Identify the parasite.
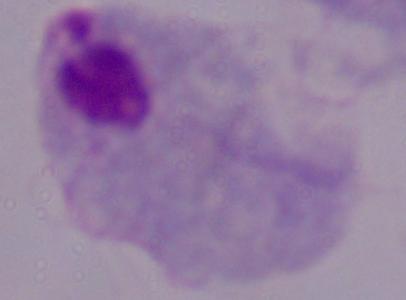

A trichomonad.

Summary:
  - Magnification: 1000x
  - Modality: photomicrograph